Describe the morphology of the erythrocytes.
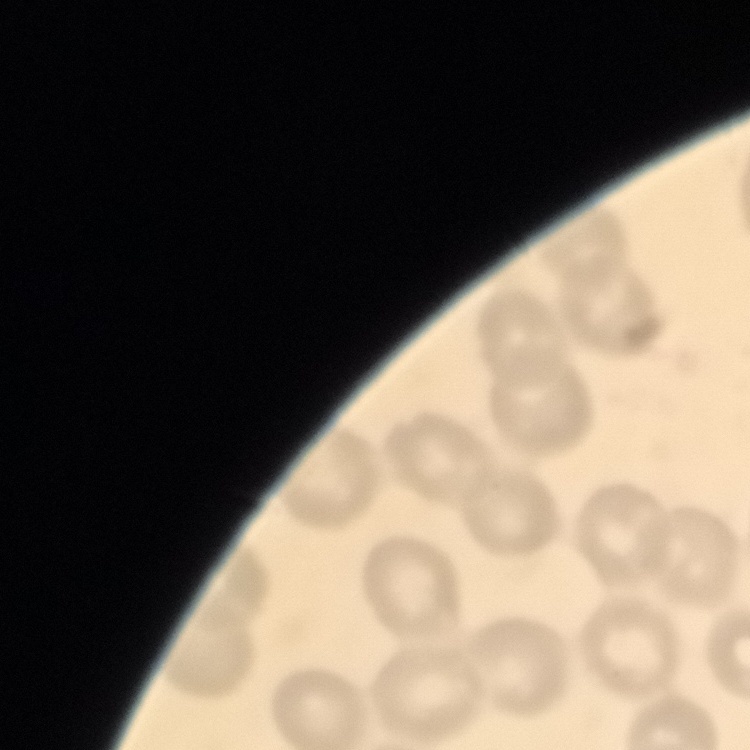
No rouleaux formation.

Summary:
  - Preparation: thin peripheral smear
  - Image type: one tile cut from a larger photomicrograph
  - Stain: Field's or Giemsa